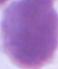
Summary:
  - Identification: red blood cell
  - Magnification: 1000x
  - Modality: micrograph